Point out each Plasmodium parasite and each leukocyte.
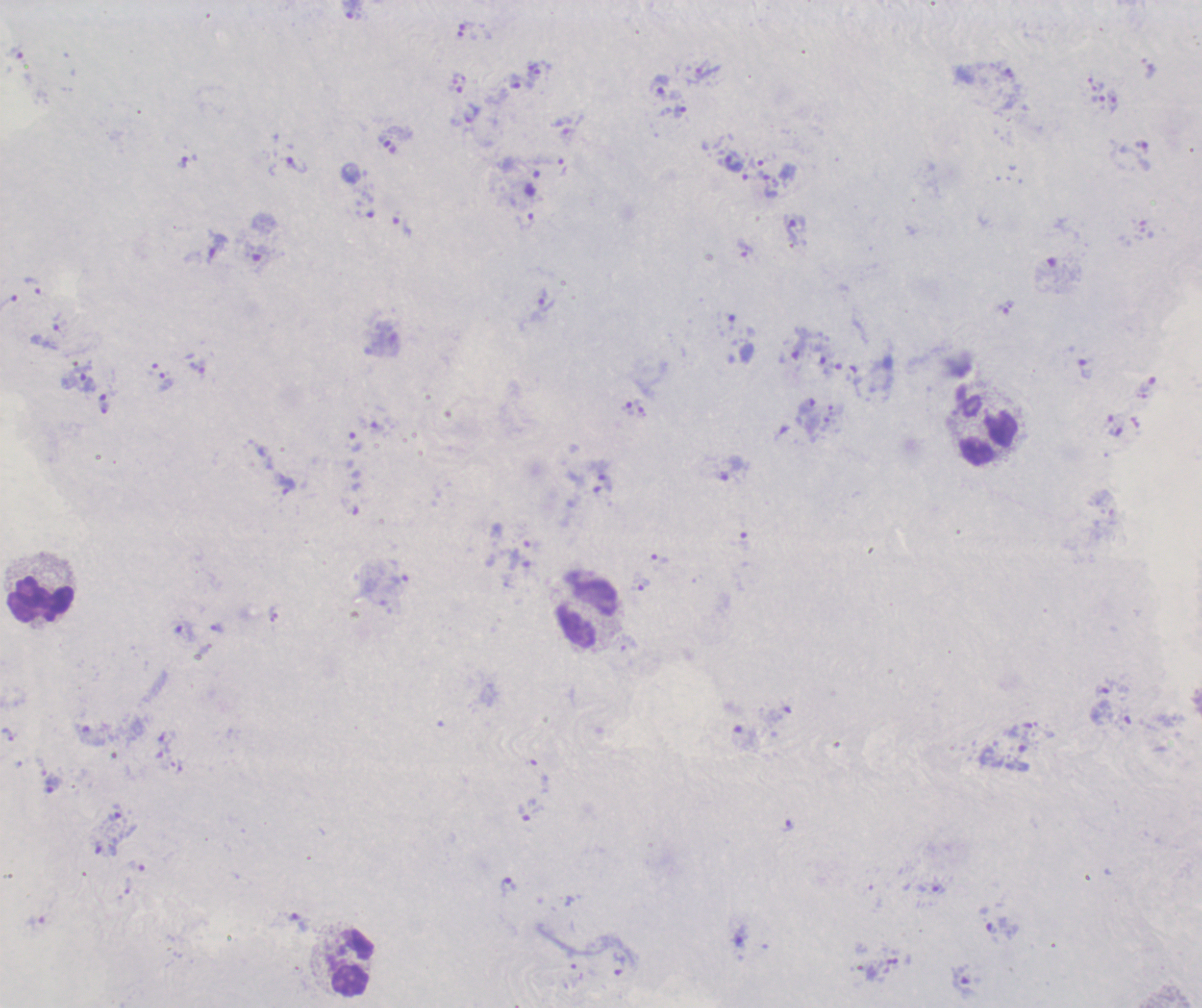
Approximate centers as [x, y] in pixels.
Trophozoites: [353, 11], [515, 82], [660, 87], [680, 111], [387, 144], [756, 162], [733, 163], [297, 165], [768, 185], [525, 221], [402, 225], [217, 248], [745, 249], [32, 286], [546, 300], [799, 344], [1085, 369], [88, 382], [731, 467], [600, 470], [640, 584], [216, 628], [185, 632], [1102, 690], [54, 784], [787, 825], [508, 887], [938, 889], [300, 923], [963, 979].
No schizont or gametocyte forms observed.
Leukocytes: [989, 438], [40, 599], [587, 613], [352, 963].

Summary:
  - Magnification: 100x
  - Preparation: thick smear of blood
  - Background quality: poor
  - Context: previously used in a real diagnosis
  - Stain: Romanowsky
  - Field of view: single
  - Image size: 1202×1008 pixels